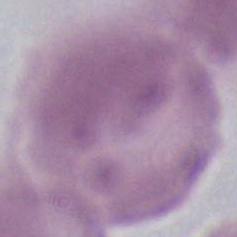

identification: erythrocyte
magnification: 1000x
modality: photomicrograph